Locate malaria parasites and leukocytes.
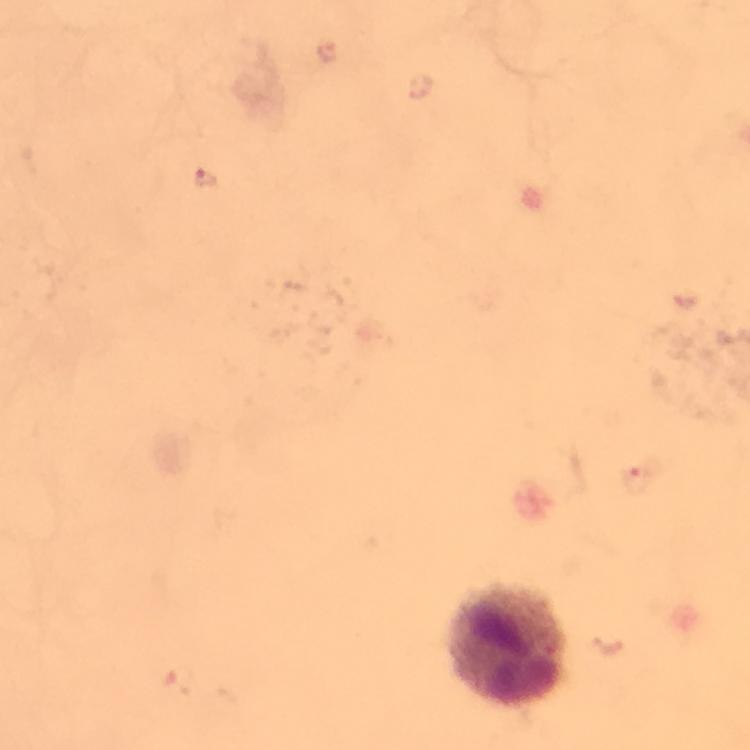
Approximate object centers, in pixels from the top-left corner.
Malaria parasites: (x=327, y=51), (x=205, y=179), (x=637, y=478), (x=180, y=679).
Leukocytes: (x=511, y=643).

Smartphone photograph taken through a microscope. From a diagnostic examination for malaria. Immersion oil applied. Thick blood film. Cropped region of a single field of view. Giemsa-stained preparation. 100x magnification. Image is 750×750 pixels.